Report the malaria status of this cell.
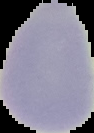

It is uninfected.

preparation = thin blood smear
image size = 94×133 pixels
image type = segmented cell region with the area outside set to black